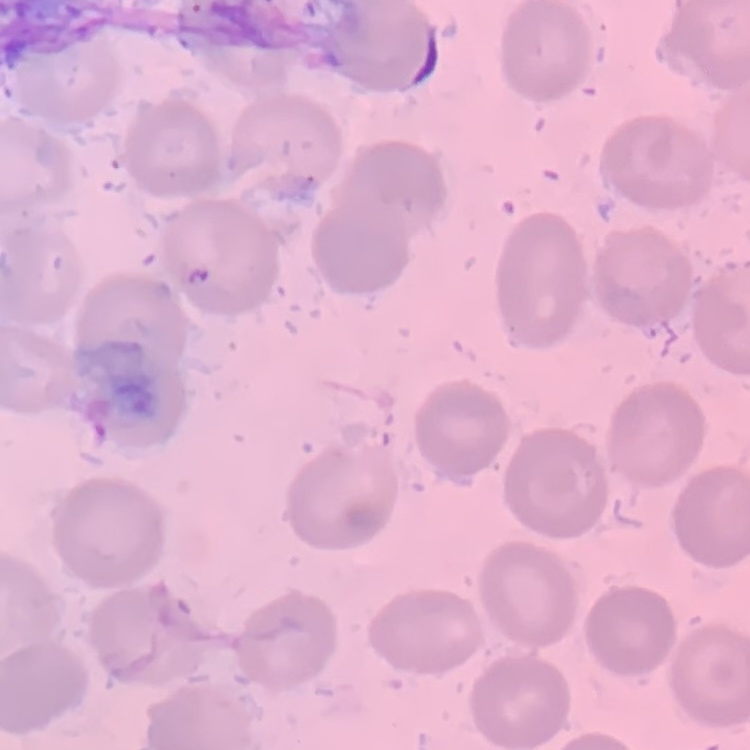

Summary:
  - Erythrocyte morphology: no rouleaux formation
  - Preparation: thin blood smear
  - Stain: Field's or Giemsa
  - Image type: one tile cut from a larger photomicrograph